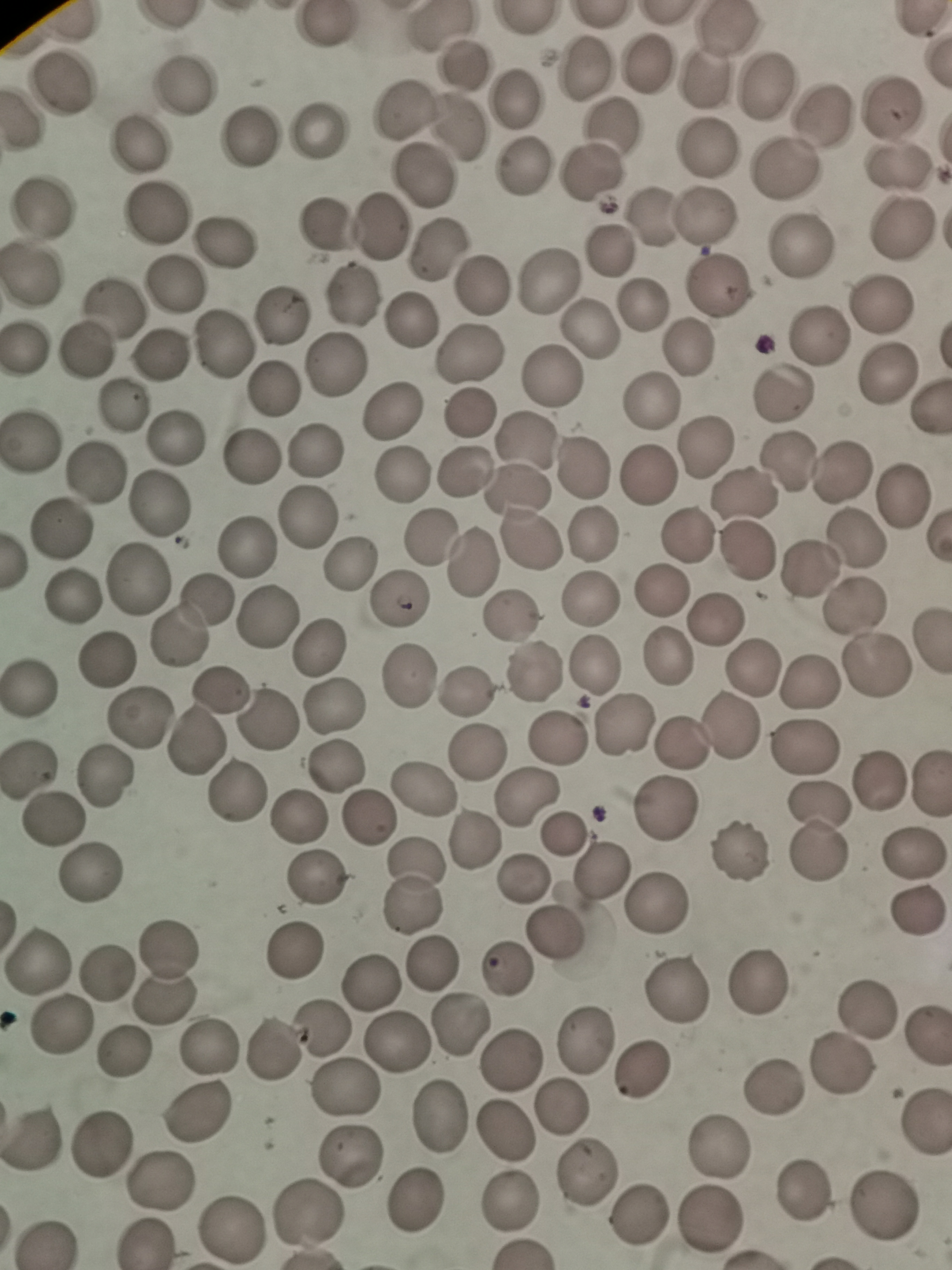
cell_locations: 'approximate centers as [x, y] in pixels: [321, 27], [438, 27], [726, 28], [648, 61], [581, 66], [468, 67], [704, 78], [62, 81], [765, 83], [185, 84], [515, 98], [893, 104], [406, 106], [825, 113], [460, 127], [613, 131], [317, 133], [248, 141], [136, 145], [710, 148], [523, 166], [895, 168], [785, 172], [591, 173], [426, 176], [44, 209], [157, 214], [651, 214], [706, 217], [381, 226], [327, 227], [900, 231], [224, 243], [437, 248], [798, 249], [609, 250], [30, 275], [547, 283], [176, 285], [479, 285], [718, 286], [353, 296], [880, 301], [643, 302], [111, 304], [280, 313], [412, 321], [591, 329], [818, 335], [222, 344], [690, 349], [87, 351], [468, 353], [162, 355], [335, 366], [887, 371], [552, 375], [273, 390], [783, 396], [649, 401], [126, 405], [471, 413], [389, 414], [31, 439], [174, 439], [525, 441], [705, 447], [315, 453], [249, 457], [792, 462], [582, 468], [465, 471], [844, 472], [94, 473], [401, 476], [648, 476], [518, 491], [744, 493], [905, 495], [160, 505], [306, 515], [58, 528], [592, 533], [687, 534], [525, 536], [859, 538], [432, 539], [248, 548], [745, 552], [348, 564], [471, 564], [811, 573], [137, 577], [659, 591], [73, 597], [203, 599], [594, 599], [398, 600], [856, 606], [266, 615], [511, 618], [715, 619], [175, 636], [319, 648], [666, 655], [104, 660], [596, 664], [751, 667], [877, 667], [531, 673], [410, 677], [31, 683], [811, 685], [467, 687], [219, 688], [334, 706], [140, 716], [264, 722], [626, 725], [732, 729], [559, 736], [682, 738], [195, 742], [804, 747], [477, 754], [337, 765], [30, 769], [106, 778], [881, 778], [425, 791], [233, 793], [528, 796], [821, 806], [669, 810], [298, 818], [367, 818], [56, 822], [562, 834], [475, 837], [740, 846], [816, 849], [914, 854], [602, 869], [90, 871], [316, 876], [525, 880], [418, 884], [659, 901], [915, 914], [556, 928], [168, 947], [296, 950], [38, 958], [433, 964], [504, 968], [109, 971], [372, 982], [755, 982], [675, 993], [164, 999], [865, 1008], [457, 1024], [59, 1027], [320, 1028], [397, 1038], [922, 1039], [583, 1042], [273, 1049], [209, 1050], [121, 1053], [512, 1062], [840, 1066], [639, 1068], [771, 1087], [348, 1089], [561, 1107], [197, 1113], [443, 1120], [923, 1126], [501, 1132], [35, 1135], [97, 1147], [716, 1147], [351, 1154], [584, 1171], [158, 1182], [804, 1190], [416, 1200], [510, 1205], [881, 1207], [304, 1216], [639, 1216], [711, 1218], [231, 1228], [49, 1241], [146, 1243]'
preparation: thin blood smear
image_size: 952×1270 pixels
field_of_view: single
stain: Giemsa
capture: smartphone camera at the microscope eyepiece